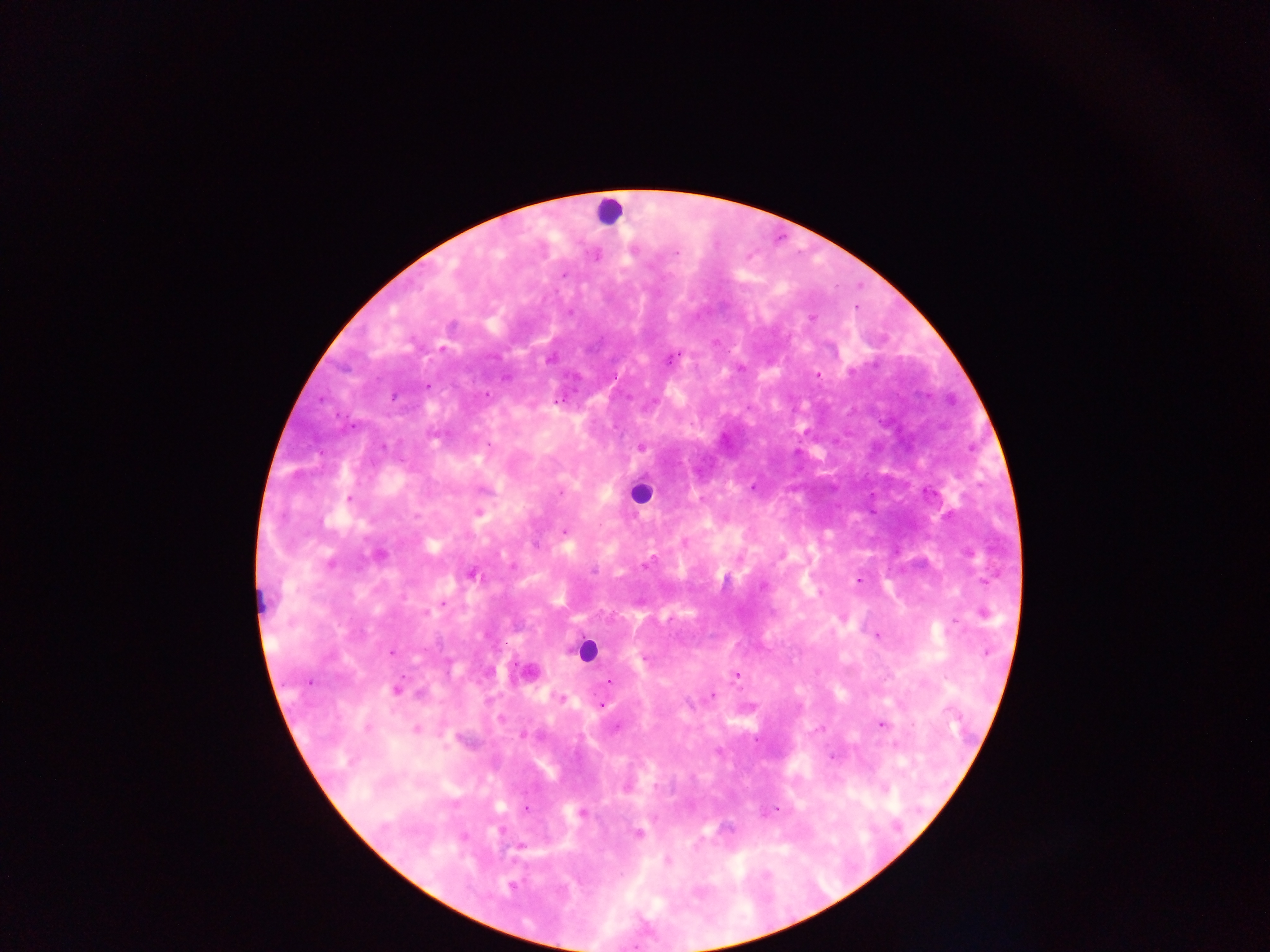
Approximate centers as {x, y} in pixels.
Summary:
  - Malaria parasite locations: {596, 255}, {856, 307}, {811, 318}, {442, 349}, {740, 367}, {817, 376}, {427, 385}, {486, 393}, {557, 399}, {641, 446}, {349, 499}, {478, 512}, {565, 532}, {685, 542}, {378, 555}, {329, 563}, {513, 566}, {472, 573}, {859, 580}, {442, 605}, {982, 612}, {842, 616}, {955, 622}, {877, 634}, {392, 652}, {528, 672}, {736, 675}, {609, 680}, {395, 690}, {712, 693}, {561, 698}, {600, 704}, {880, 724}, {415, 729}, {831, 756}, {626, 786}, {882, 788}, {525, 808}, {581, 813}, {637, 834}, {519, 845}, {668, 861}, {512, 886}
  - Leukocyte locations: {608, 211}, {638, 494}, {585, 651}
  - Capture: mobile-phone photograph through a microscope
  - Field of view: single
  - Preparation: thick blood smear
  - Country: Ghana
  - Image size: 1270×952 pixels